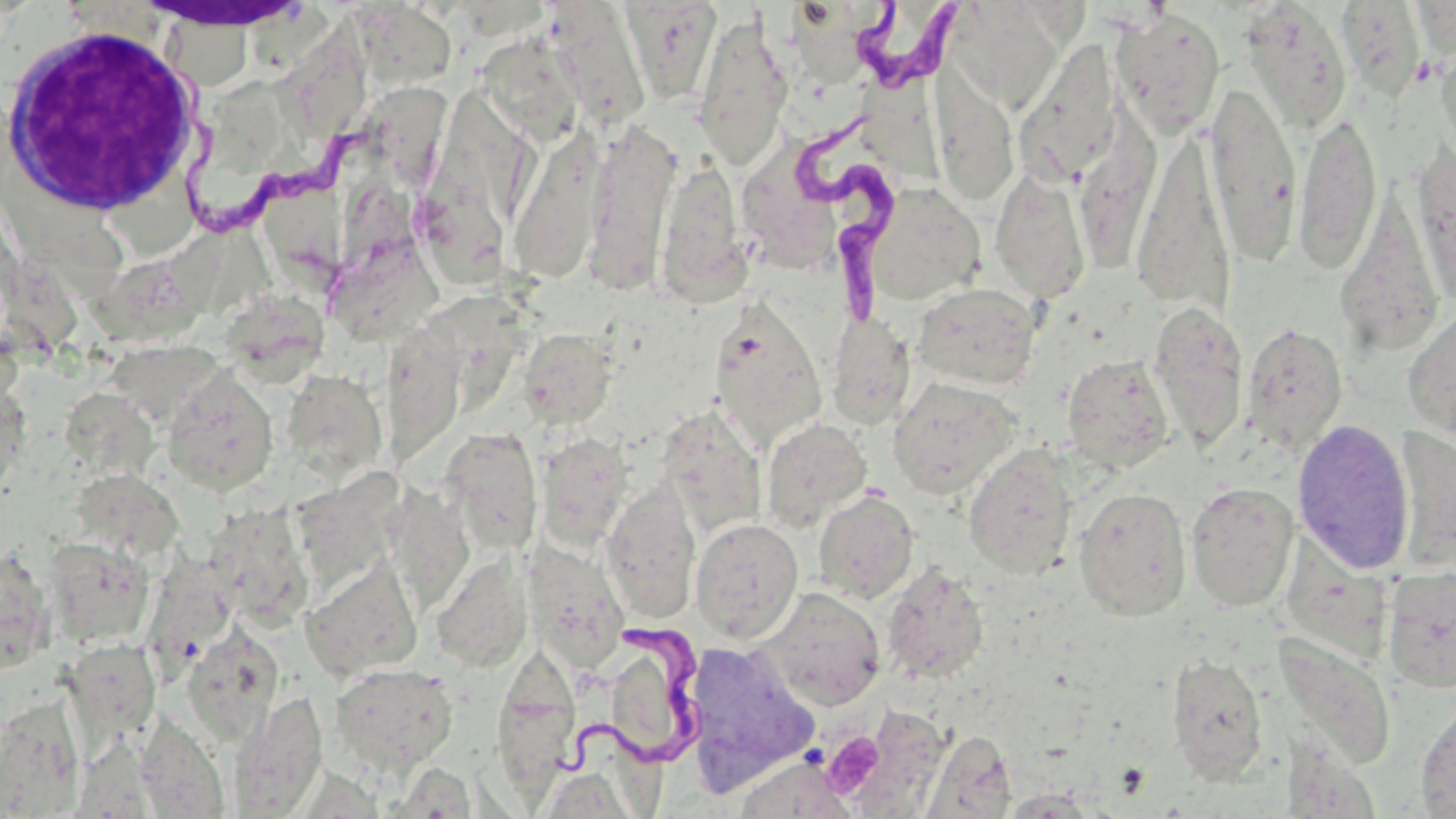
slide-level diagnosis = Trypanosoma brucei
uninfected red blood cell locations = approximate bounding boxes as (x1, y1, x2, y2) in pixels: (949, 1, 1063, 112), (1335, 1, 1426, 100), (616, 2, 721, 105), (1241, 3, 1353, 133), (347, 5, 456, 81), (546, 6, 653, 132), (149, 9, 272, 77), (1112, 9, 1226, 138), (692, 14, 792, 169), (294, 30, 373, 136), (477, 35, 584, 142), (1016, 43, 1125, 187), (1435, 43, 1456, 164), (932, 73, 1021, 205), (1206, 83, 1301, 261), (212, 92, 296, 182), (375, 93, 460, 204), (1293, 109, 1382, 275), (583, 123, 679, 295), (509, 131, 606, 284), (1132, 132, 1236, 317), (429, 143, 516, 286), (1412, 145, 1456, 308), (657, 158, 751, 307), (989, 168, 1092, 303), (864, 183, 985, 307), (273, 196, 359, 296), (1336, 196, 1446, 358), (7, 199, 127, 302), (355, 212, 437, 342), (172, 238, 283, 336), (96, 259, 205, 345), (912, 282, 1041, 391), (232, 290, 332, 389), (460, 290, 524, 400), (711, 298, 827, 450), (1401, 301, 1456, 442), (1148, 302, 1247, 452), (827, 311, 915, 431), (1242, 323, 1348, 453), (519, 329, 617, 429), (389, 341, 473, 460), (107, 342, 213, 422), (1062, 354, 1175, 472), (162, 366, 279, 497), (282, 369, 388, 482), (0, 375, 30, 505), (889, 377, 1020, 499), (70, 393, 162, 485), (657, 406, 766, 537), (762, 418, 872, 531), (1292, 418, 1416, 574), (1393, 424, 1456, 576), (440, 428, 544, 556), (537, 432, 634, 550), (963, 444, 1077, 578), (298, 470, 413, 586), (391, 472, 476, 604), (62, 474, 180, 569), (602, 481, 701, 623), (1185, 481, 1300, 612), (1074, 487, 1192, 621), (813, 490, 919, 604), (224, 506, 326, 637), (690, 517, 803, 643), (44, 536, 156, 647), (524, 543, 629, 670), (0, 544, 57, 671), (431, 552, 533, 673), (145, 557, 251, 683), (303, 559, 424, 680), (880, 562, 989, 685), (1382, 566, 1456, 693), (760, 587, 886, 710), (181, 623, 282, 746), (1277, 635, 1399, 771), (683, 640, 819, 790), (489, 647, 584, 797), (607, 650, 672, 819), (1166, 653, 1270, 785), (59, 659, 178, 750), (329, 662, 458, 774), (229, 692, 328, 816), (0, 696, 85, 817), (1414, 699, 1456, 818), (837, 706, 950, 816), (138, 711, 231, 819), (83, 721, 158, 819), (924, 730, 1017, 818), (731, 755, 855, 819), (385, 761, 472, 818), (996, 789, 1104, 817)
stain = May-Grünwald-Giemsa
platelet locations = approximate bounding boxes as (x1, y1, x2, y2) in pixels: (822, 732, 885, 798)
image size = 1456×819 pixels
white blood cell locations = approximate bounding boxes as (x1, y1, x2, y2) in pixels: (137, 0, 306, 31), (0, 22, 206, 220)
preparation = thin blood film
Trypanosoma brucei locations = approximate bounding boxes as (x1, y1, x2, y2) in pixels: (853, 3, 967, 93), (172, 53, 374, 229), (783, 121, 894, 321), (550, 615, 706, 782)
modality = optical microscopy
magnification = 1000x
field of view = single